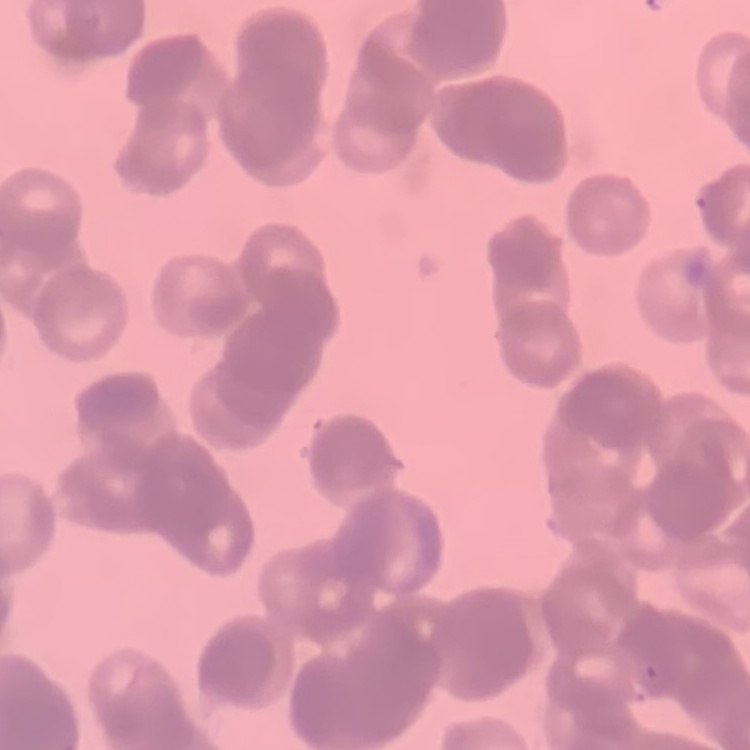
red blood cell morphology = rouleaux formation
stain = Field's or Giemsa
preparation = thin blood smear
image type = square crop of a larger photomicrograph